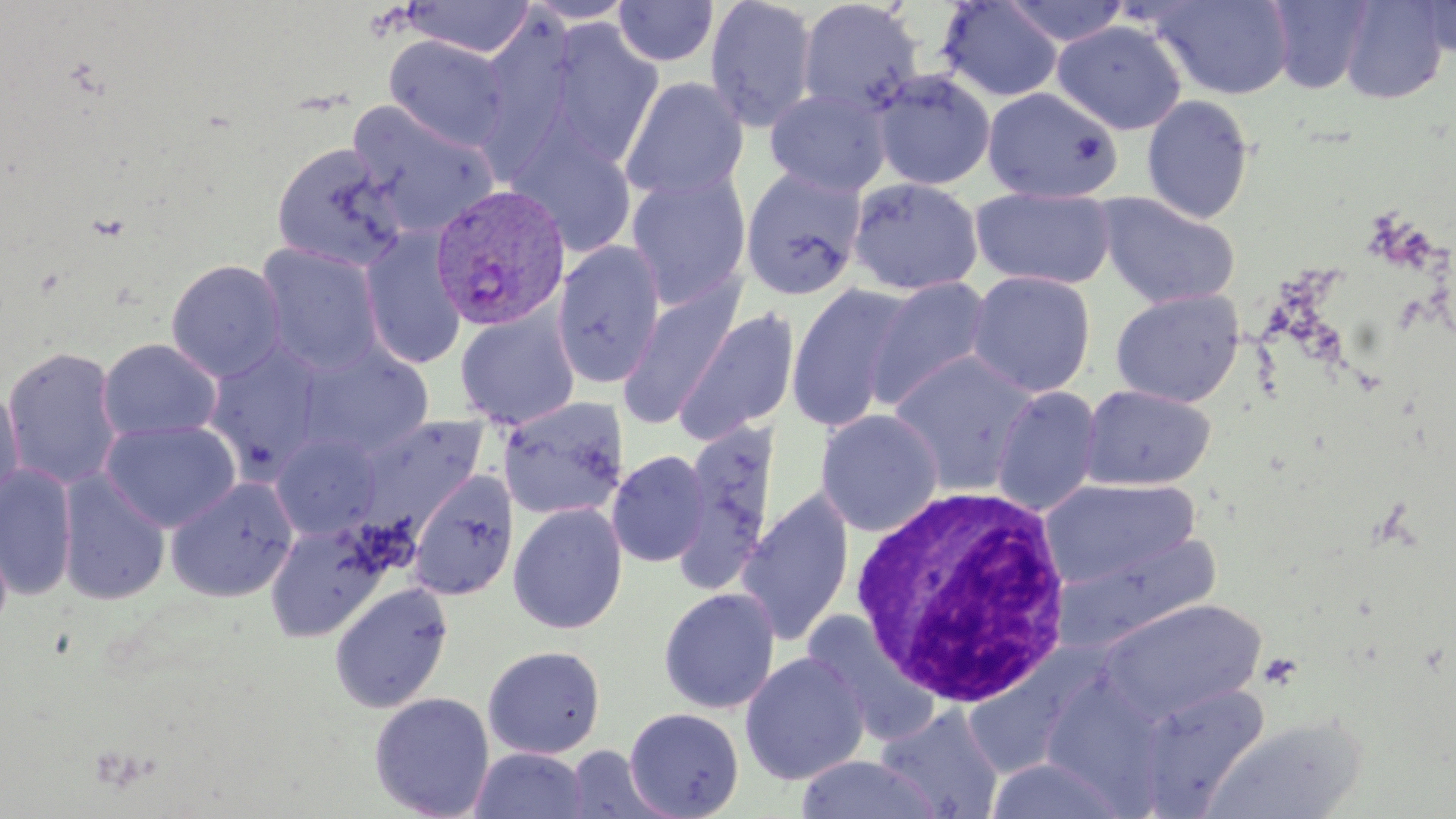
Summary:
  - Coordinate format: approximate bounding boxes as named x1/y1/x2/y2 corners in pixels
  - White blood cell locations: (x1=849, y1=486, x2=1073, y2=707)
  - Uninfected red blood cell locations: (x1=613, y1=0, x2=719, y2=67), (x1=704, y1=0, x2=818, y2=133), (x1=797, y1=0, x2=925, y2=117), (x1=1147, y1=0, x2=1295, y2=100), (x1=1264, y1=0, x2=1375, y2=94), (x1=1339, y1=0, x2=1451, y2=104), (x1=1413, y1=0, x2=1456, y2=59), (x1=403, y1=1, x2=535, y2=58), (x1=519, y1=1, x2=638, y2=25), (x1=936, y1=1, x2=1065, y2=102), (x1=1000, y1=1, x2=1132, y2=48), (x1=475, y1=17, x2=580, y2=171), (x1=545, y1=20, x2=664, y2=167), (x1=1052, y1=20, x2=1188, y2=135), (x1=384, y1=35, x2=510, y2=151), (x1=871, y1=69, x2=996, y2=191), (x1=620, y1=76, x2=749, y2=201), (x1=981, y1=86, x2=1124, y2=203), (x1=764, y1=87, x2=892, y2=196), (x1=1141, y1=94, x2=1255, y2=224), (x1=346, y1=99, x2=501, y2=236), (x1=508, y1=130, x2=638, y2=258), (x1=270, y1=143, x2=408, y2=272), (x1=740, y1=168, x2=867, y2=300), (x1=625, y1=171, x2=751, y2=309), (x1=847, y1=177, x2=984, y2=296), (x1=969, y1=188, x2=1118, y2=290), (x1=1095, y1=192, x2=1241, y2=309), (x1=360, y1=229, x2=467, y2=370), (x1=552, y1=240, x2=666, y2=388), (x1=256, y1=243, x2=385, y2=375), (x1=165, y1=259, x2=287, y2=382), (x1=966, y1=270, x2=1096, y2=397), (x1=865, y1=275, x2=994, y2=411), (x1=617, y1=279, x2=746, y2=430), (x1=785, y1=284, x2=912, y2=432), (x1=1109, y1=289, x2=1246, y2=407), (x1=673, y1=308, x2=800, y2=443), (x1=455, y1=310, x2=579, y2=429), (x1=97, y1=338, x2=222, y2=442), (x1=203, y1=342, x2=329, y2=478), (x1=296, y1=343, x2=434, y2=459), (x1=2, y1=345, x2=124, y2=490), (x1=888, y1=350, x2=1039, y2=494), (x1=1079, y1=383, x2=1216, y2=491), (x1=0, y1=384, x2=24, y2=511), (x1=990, y1=386, x2=1103, y2=516), (x1=497, y1=397, x2=629, y2=521), (x1=815, y1=409, x2=944, y2=537), (x1=352, y1=415, x2=488, y2=535), (x1=100, y1=419, x2=242, y2=533), (x1=673, y1=420, x2=782, y2=595), (x1=270, y1=432, x2=383, y2=540), (x1=606, y1=450, x2=710, y2=568), (x1=0, y1=464, x2=78, y2=601), (x1=407, y1=468, x2=520, y2=601), (x1=56, y1=469, x2=171, y2=605), (x1=1040, y1=476, x2=1201, y2=590), (x1=166, y1=477, x2=299, y2=602), (x1=736, y1=490, x2=856, y2=646), (x1=507, y1=502, x2=629, y2=635), (x1=264, y1=521, x2=388, y2=642), (x1=1054, y1=530, x2=1223, y2=650), (x1=328, y1=582, x2=454, y2=713), (x1=658, y1=587, x2=780, y2=714), (x1=1098, y1=599, x2=1266, y2=723), (x1=482, y1=644, x2=606, y2=759), (x1=739, y1=650, x2=870, y2=785), (x1=1132, y1=682, x2=1270, y2=814), (x1=368, y1=691, x2=495, y2=819), (x1=875, y1=705, x2=1005, y2=818), (x1=624, y1=707, x2=745, y2=818), (x1=1203, y1=716, x2=1367, y2=819), (x1=564, y1=746, x2=673, y2=818), (x1=469, y1=747, x2=590, y2=819), (x1=795, y1=754, x2=945, y2=819), (x1=983, y1=758, x2=1134, y2=817)
  - Plasmodium vivax-infected red blood cell locations: (x1=428, y1=182, x2=572, y2=334)
  - Slide-level diagnosis: Plasmodium vivax
  - Modality: optical microscopy
  - Magnification: 1000x
  - Preparation: thin blood film
  - Field of view: one of a larger specimen
  - Image size: 1456×819 pixels
  - Stain: May-Grünwald-Giemsa